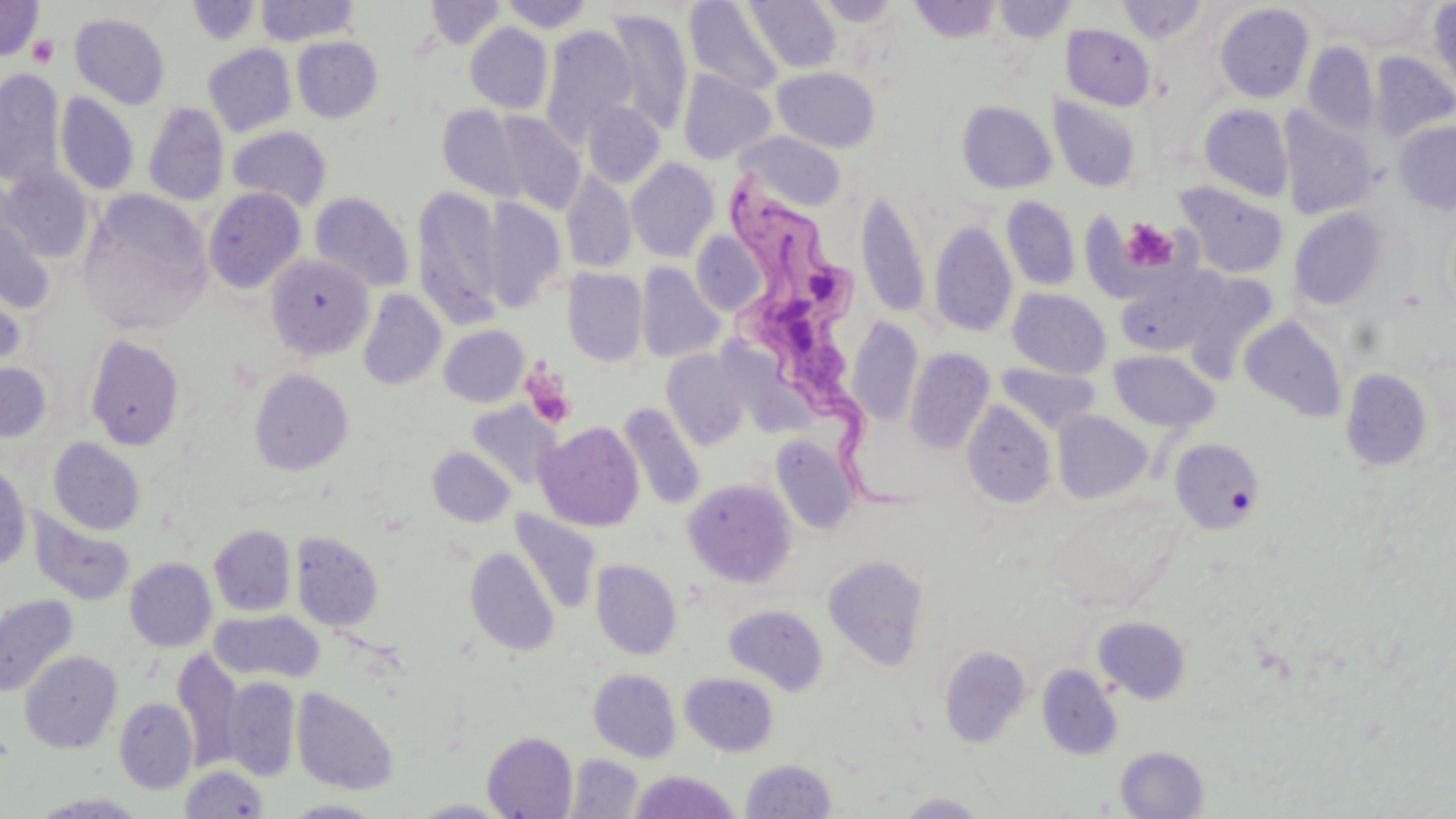
Summary:
  - Coordinate format: approximate bounding boxes as (x1, y1, x2, y2) in pixels
  - Platelet locations: (27, 33, 59, 67), (1120, 218, 1178, 273), (522, 369, 576, 430)
  - Uninfected red blood cell locations: (0, 0, 43, 60), (186, 0, 259, 44), (255, 0, 360, 45), (498, 0, 595, 32), (746, 0, 841, 73), (812, 0, 905, 26), (994, 0, 1076, 42), (1118, 0, 1208, 43), (425, 1, 506, 49), (910, 1, 1001, 43), (1338, 1, 1432, 52), (684, 2, 785, 95), (1429, 2, 1456, 95), (1215, 3, 1315, 103), (604, 7, 694, 135), (70, 13, 171, 109), (466, 23, 553, 114), (1061, 24, 1156, 110), (540, 26, 637, 147), (292, 36, 383, 122), (1303, 43, 1379, 136), (203, 45, 295, 137), (1370, 52, 1456, 141), (772, 67, 880, 153), (0, 69, 64, 189), (678, 69, 776, 164), (56, 93, 138, 195), (1050, 96, 1143, 192), (582, 100, 664, 188), (957, 101, 1057, 194), (143, 102, 229, 206), (1200, 104, 1294, 201), (438, 105, 529, 202), (1279, 108, 1378, 220), (492, 110, 584, 214), (1394, 121, 1456, 214), (228, 126, 332, 211), (737, 132, 846, 210), (627, 158, 720, 261), (2, 167, 94, 262), (562, 170, 637, 274), (1174, 181, 1289, 279), (412, 186, 504, 330), (203, 188, 305, 294), (856, 189, 930, 319), (79, 190, 212, 334), (310, 191, 415, 292), (0, 192, 56, 314), (1002, 196, 1080, 290), (483, 197, 566, 312), (1288, 207, 1388, 310), (929, 221, 1018, 338), (691, 232, 766, 316), (266, 254, 374, 360), (636, 262, 725, 363), (1115, 263, 1230, 358), (564, 268, 649, 367), (1184, 273, 1280, 380), (0, 277, 26, 374), (1008, 288, 1112, 378), (358, 289, 446, 390), (1239, 316, 1347, 422), (846, 317, 924, 427), (439, 325, 529, 407), (85, 335, 186, 450), (905, 347, 995, 454), (662, 349, 751, 450), (1110, 349, 1220, 433), (905, 352, 1097, 446), (0, 361, 53, 442), (996, 363, 1099, 433), (1340, 367, 1434, 471), (249, 369, 353, 475), (962, 400, 1056, 508), (618, 402, 706, 511), (468, 404, 559, 490), (1053, 411, 1151, 502), (536, 422, 644, 531), (771, 435, 860, 535), (48, 437, 145, 535), (1169, 437, 1266, 534), (427, 446, 516, 527), (0, 463, 31, 570), (683, 478, 797, 587), (28, 511, 135, 606), (511, 511, 601, 616), (209, 525, 296, 616), (290, 531, 383, 632), (465, 547, 559, 656), (823, 554, 928, 670), (125, 558, 216, 651), (591, 560, 681, 659), (0, 593, 79, 698), (724, 604, 829, 695), (210, 610, 323, 683), (1093, 616, 1192, 704), (940, 646, 1033, 747), (173, 649, 242, 773), (20, 651, 122, 753), (1037, 663, 1123, 760), (588, 669, 681, 762), (681, 673, 779, 756), (223, 677, 300, 781), (292, 687, 399, 795), (114, 698, 198, 793), (482, 731, 578, 818), (1115, 745, 1209, 818), (564, 754, 643, 817), (741, 759, 836, 818), (179, 765, 268, 818), (629, 770, 742, 818), (31, 792, 149, 818), (895, 793, 991, 818), (409, 799, 513, 818), (282, 800, 386, 818)
  - Trypanosoma brucei locations: (717, 172, 924, 525)
  - Slide-level diagnosis: Trypanosoma brucei
  - Stain: May-Grünwald-Giemsa
  - Field of view: one of a larger specimen
  - Modality: optical microscopy
  - Preparation: thin blood smear
  - Magnification: 1000x
  - Image size: 1456×819 pixels